Report the malaria status of this cell.
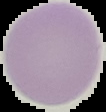
Uninfected.

Summary:
  - Image type: segmented cell region with the area outside set to black
  - Image size: 106×112 pixels
  - Preparation: thin blood smear